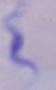

Summary:
  - Identification: trypanosome
  - Magnification: 1000x
  - Modality: photomicrograph